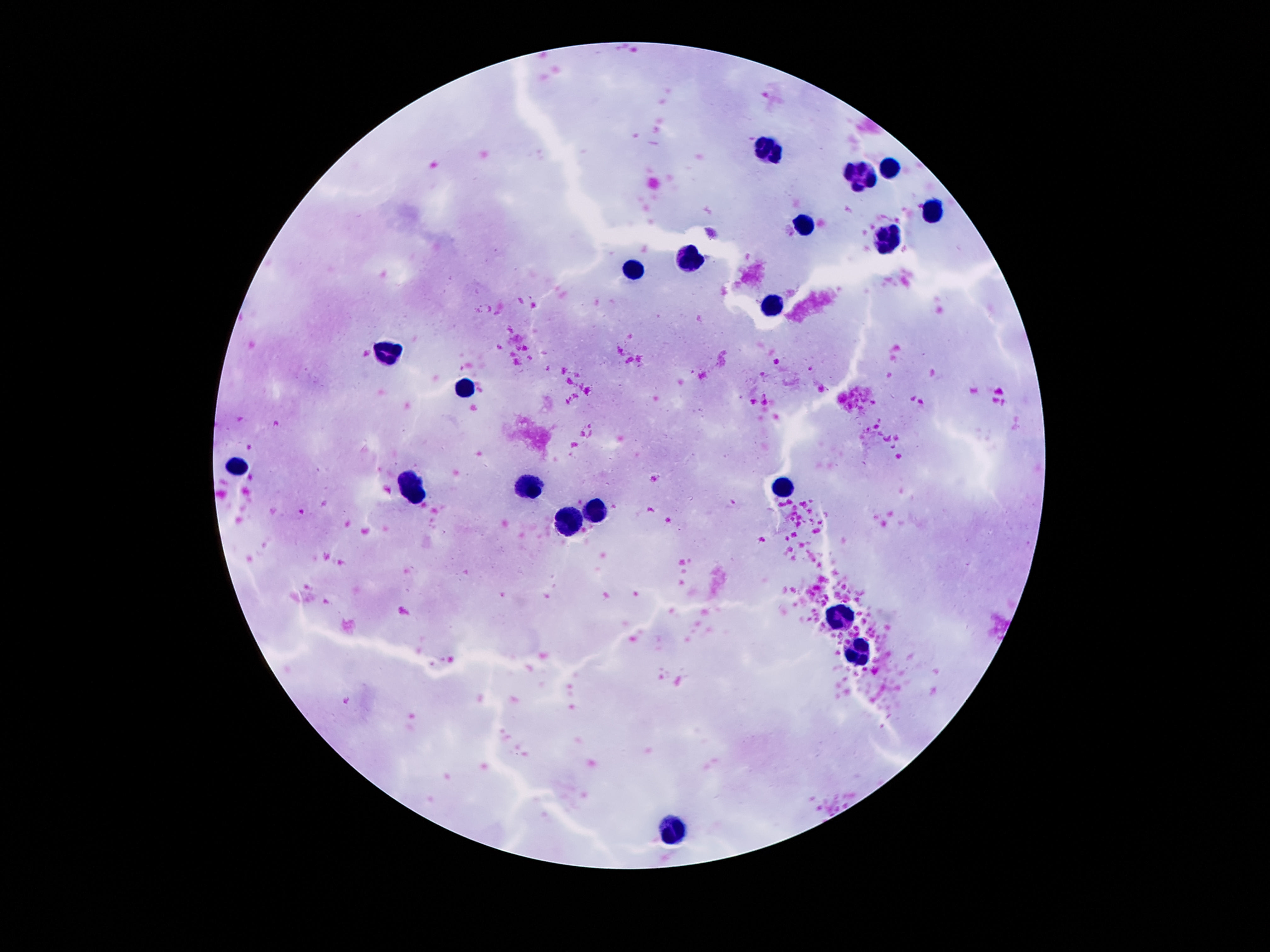

{
  "stain": "Giemsa",
  "field_of_view": "single",
  "capture": "smartphone camera through the microscope eyepiece",
  "patient_malaria_status": "not infected",
  "preparation": "thick blood film",
  "leukocyte_locations": "approximate object centers, in pixels from the top-left corner: (x=770, y=147), (x=890, y=170), (x=863, y=178), (x=932, y=209), (x=801, y=226), (x=887, y=238), (x=693, y=258), (x=638, y=268), (x=774, y=306), (x=383, y=351), (x=467, y=389), (x=239, y=464), (x=788, y=486), (x=414, y=488), (x=529, y=488), (x=595, y=511), (x=573, y=520), (x=839, y=617), (x=858, y=654), (x=673, y=827)",
  "magnification": "100x",
  "image_size": "1270×952 pixels"
}